Locate every Plasmodium parasite and every leukocyte.
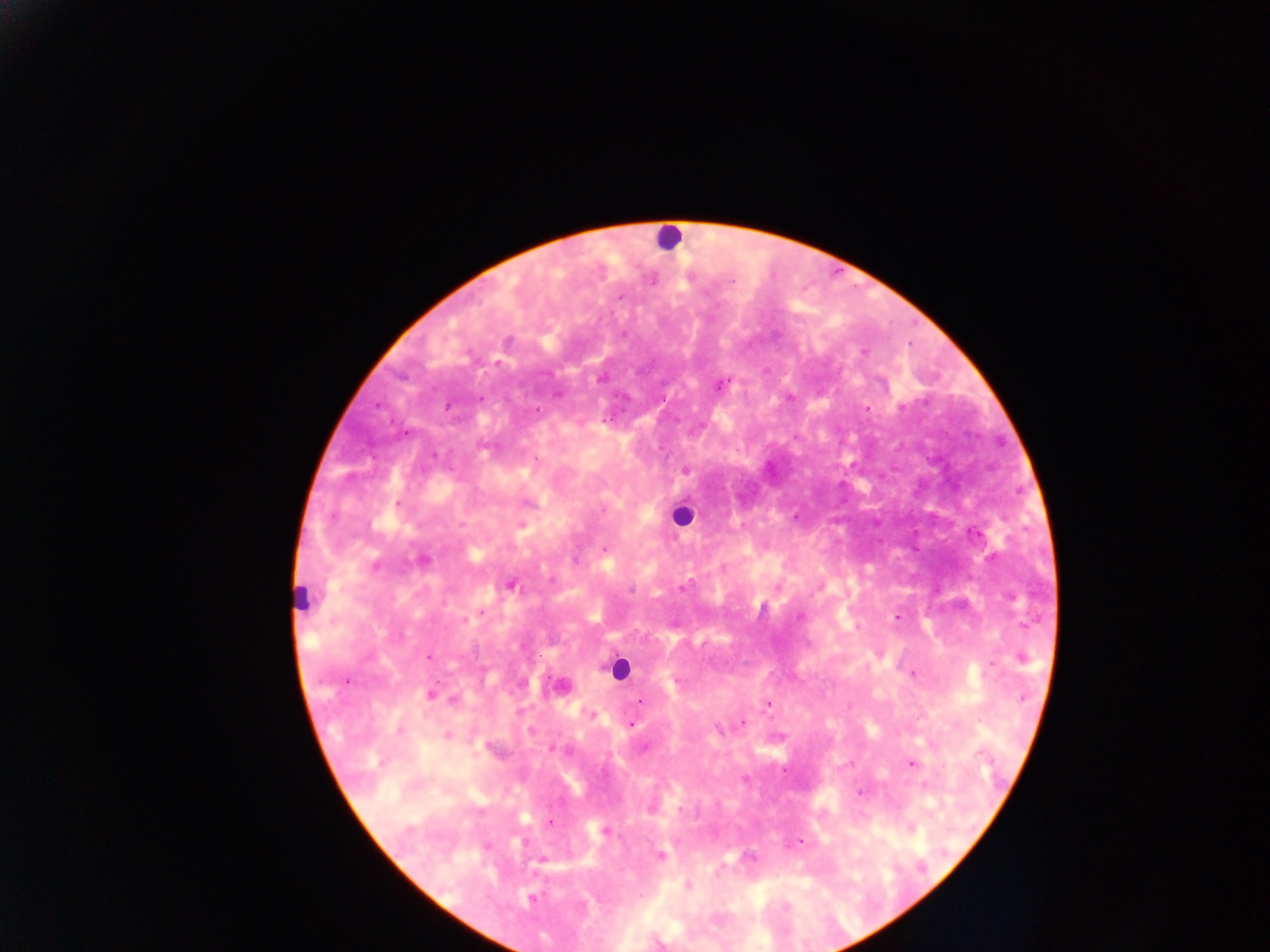

Approximate centers as x y in pixels.
Plasmodium parasites: 653 281; 619 297; 624 334; 508 341; 863 352; 497 363; 600 379; 720 384; 789 397; 480 398; 446 406; 901 407; 867 409; 537 410; 407 433; 434 455; 684 470; 398 504; 603 510; 521 525; 605 549; 422 560; 574 561; 375 565; 551 580; 511 585; 683 588; 631 589; 482 612; 798 617; 897 617; 463 620; 429 657; 1022 658; 992 666; 912 674; 432 694; 1023 697; 453 700; 640 701; 768 703; 592 714; 742 722; 630 724; 400 730; 531 731; 447 736; 553 748; 645 748; 981 754; 911 763; 851 764; 942 767; 861 793; 549 823; 605 832; 524 842; 800 842; 661 856; 542 860; 687 886; 532 898.
Leukocytes: 668 237; 682 516; 301 600; 617 669.

Summary:
  - Country: Ghana
  - Field of view: single
  - Capture: mobile-phone photograph through a microscope
  - Preparation: thick blood smear
  - Image size: 1270×952 pixels